Locate every Trypanosoma brucei.
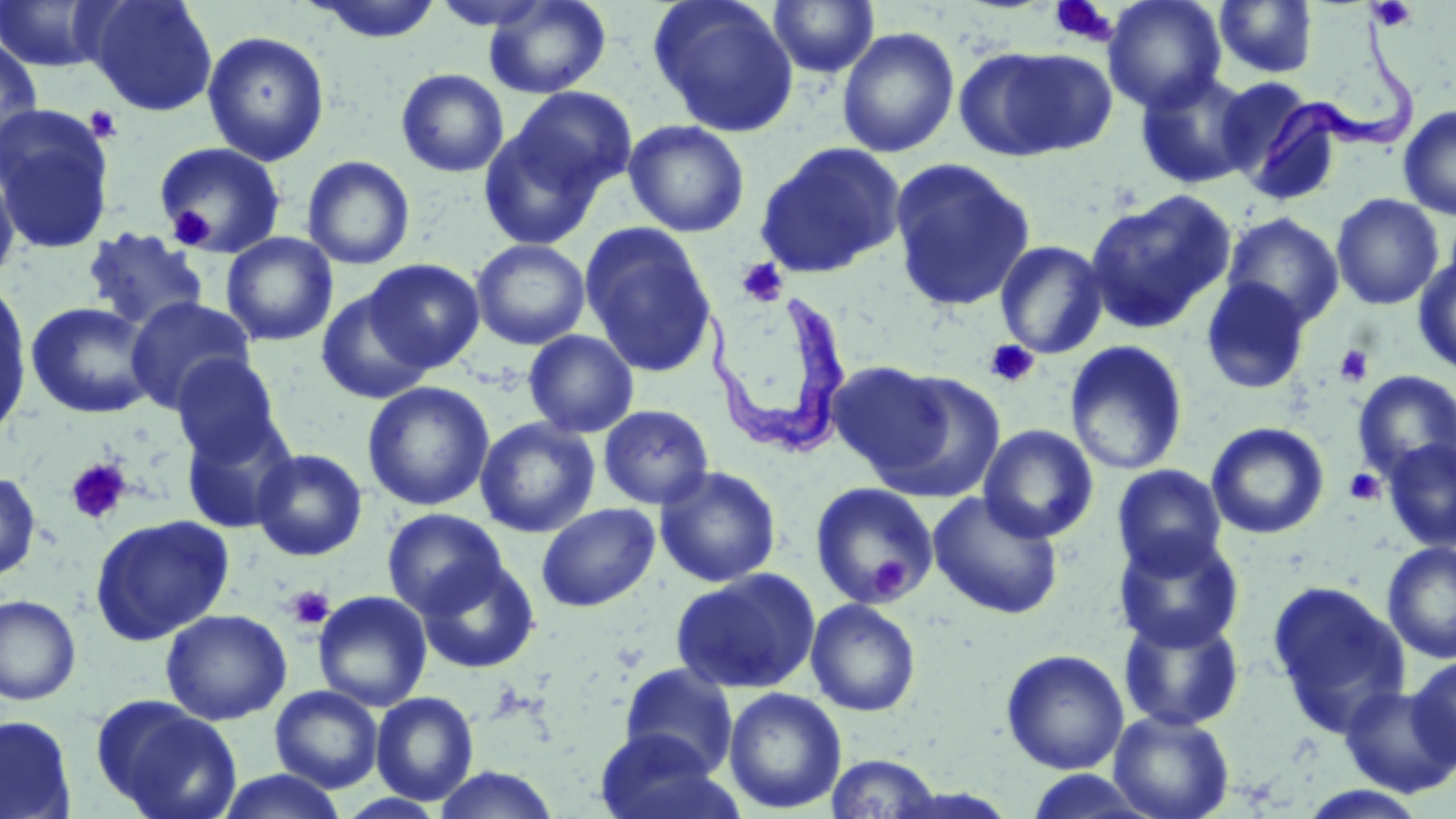
Approximate bounding boxes as [x1, y1, x2, y2] in pixels.
Trypanosoma brucei: [1259, 16, 1416, 179], [708, 289, 854, 461].

Uninfected red blood cell locations: [84, 0, 218, 117], [304, 0, 444, 43], [483, 0, 612, 99], [648, 0, 799, 137], [1103, 0, 1227, 113], [0, 1, 118, 73], [768, 1, 879, 78], [1213, 1, 1318, 79], [836, 27, 960, 158], [202, 30, 330, 165], [0, 36, 44, 162], [957, 45, 1111, 160], [396, 68, 509, 177], [1134, 69, 1258, 189], [1214, 77, 1330, 193], [503, 86, 638, 207], [1397, 104, 1456, 220], [0, 106, 116, 254], [477, 116, 611, 251], [623, 119, 750, 237], [153, 141, 286, 258], [754, 142, 907, 279], [0, 154, 21, 289], [302, 155, 415, 270], [889, 157, 1036, 312], [1084, 189, 1236, 333], [1331, 193, 1445, 310], [1220, 212, 1344, 329], [579, 223, 718, 379], [82, 227, 210, 333], [220, 232, 338, 346], [471, 239, 591, 350], [995, 239, 1109, 359], [1413, 255, 1456, 376], [363, 258, 484, 371], [1199, 277, 1311, 395], [0, 282, 33, 437], [315, 289, 435, 405], [125, 297, 256, 413], [26, 301, 159, 419], [523, 329, 639, 438], [1064, 341, 1188, 475], [171, 354, 283, 464], [826, 360, 951, 476], [869, 370, 1007, 502], [1352, 370, 1456, 486], [362, 381, 494, 511], [598, 404, 714, 510], [180, 414, 298, 533], [475, 417, 600, 537], [1206, 422, 1329, 539], [978, 425, 1098, 543], [1382, 437, 1456, 552], [251, 448, 368, 561], [1112, 463, 1227, 577], [654, 466, 781, 588], [0, 470, 42, 583], [810, 482, 939, 609], [928, 491, 1063, 620], [537, 503, 660, 611], [382, 508, 507, 618], [90, 514, 234, 644], [1113, 530, 1245, 653], [1382, 541, 1456, 664], [416, 557, 540, 673], [670, 568, 821, 694], [1267, 580, 1411, 736], [313, 590, 432, 711], [0, 594, 82, 705], [805, 598, 921, 717], [160, 608, 292, 725], [1118, 611, 1245, 731], [1001, 648, 1129, 774], [1408, 653, 1456, 770], [619, 662, 739, 777], [1340, 684, 1456, 798], [270, 685, 384, 792], [723, 687, 847, 814], [370, 691, 479, 805], [94, 697, 242, 819], [1108, 710, 1234, 819], [0, 714, 77, 819], [595, 729, 732, 819], [824, 753, 943, 818], [431, 765, 562, 819], [213, 769, 350, 819], [1022, 770, 1162, 818], [1297, 786, 1433, 819]. Platelet locations: [1368, 0, 1417, 32], [1050, 1, 1119, 46], [84, 105, 124, 144], [167, 205, 215, 250], [735, 258, 789, 307], [985, 339, 1039, 388], [1334, 343, 1375, 387], [65, 458, 132, 526], [1345, 468, 1385, 505], [871, 556, 909, 595], [285, 585, 335, 630]. Slide-level diagnosis: Trypanosoma brucei. Thin blood film. May-Grünwald-Giemsa stain. One field of a larger specimen. 1000x magnification. Light microscopy. Image is 1456×819 pixels.